Classify this cell by malaria status.
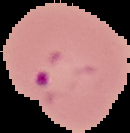
It is parasitized.

image_size: 130×133 pixels
image_type: segmented cell region on a black background
preparation: thin blood film